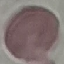 Malaria status: uninfected. Cell patch, automatically extracted from a larger field of view and resized to 64 × 64 pixels. Giemsa-stained preparation. Photographed with a smartphone camera at the microscope eyepiece. Thin smear of blood.